Classify this cell by malaria status.
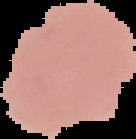
Uninfected.

Summary:
  - Preparation: thin blood smear
  - Image size: 136×139 pixels
  - Image type: cell region segmented out of the field of view; surrounding area masked to black